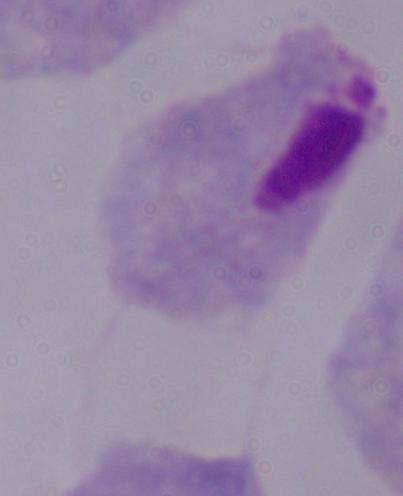 A trichomonad is shown. 1000x magnification. Micrograph.